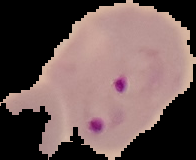

image_type: segmented cell region on a black background
malaria_status: parasitized
preparation: thin blood smear
image_size: 196×160 pixels